State which cell type is depicted.
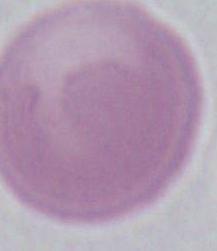
This is an erythrocyte.

1000x magnification. Photomicrograph.